Assess this cell for malaria.
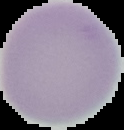
It is uninfected.

preparation = thin blood smear
image size = 124×130 pixels
image type = cell region segmented out of the field of view; surrounding area masked to black